Name the parasite shown.
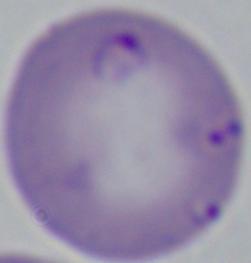

Babesia.

Photomicrograph. Captured at 1000x magnification.